Assess the background quality.
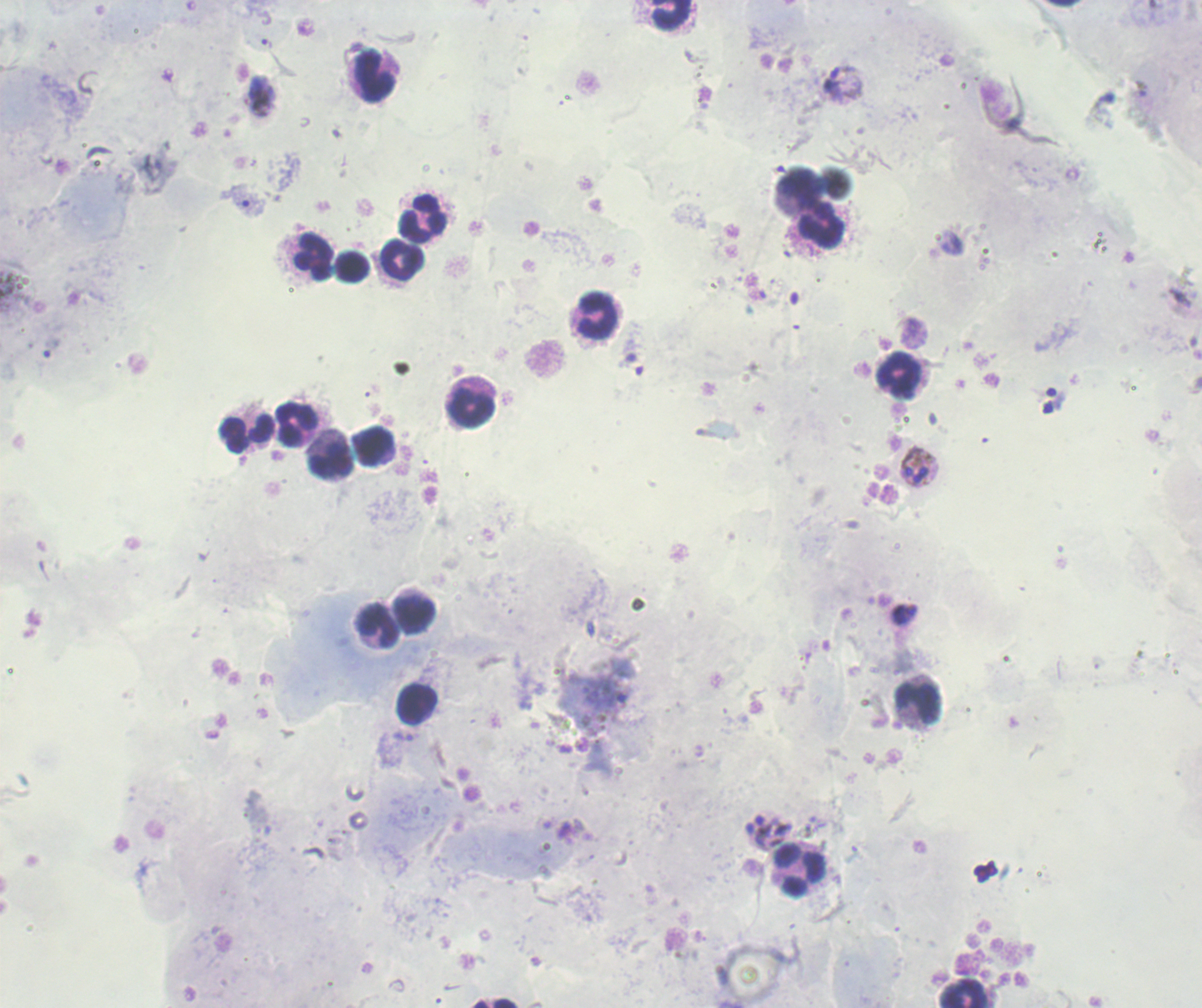

Unsatisfactory.

life_cycle_stages_observed: trophozoite, schizont
field_of_view: single
image_size: 1202×1008 pixels
stain: Romanowsky
leukocyte_locations: 'approximate object centers, in pixels from the top-left corner: (x=672, y=15), (x=371, y=76), (x=801, y=192), (x=424, y=220), (x=821, y=227), (x=314, y=258), (x=402, y=261), (x=353, y=268), (x=596, y=316), (x=899, y=375), (x=469, y=406), (x=295, y=427), (x=246, y=434), (x=376, y=448), (x=332, y=459), (x=414, y=612), (x=378, y=627), (x=917, y=702), (x=417, y=704), (x=799, y=870), (x=964, y=994)'
context: previously used in a real diagnosis
result: malaria parasites detected
trophozoite_locations: 'approximate object centers, in pixels from the top-left corner: (x=266, y=43), (x=844, y=85), (x=262, y=97)'
schizont_locations: 'approximate object centers, in pixels from the top-left corner: (x=919, y=467), (x=769, y=830)'
magnification: 100x
preparation: thick smear of blood